Assess this cell for malaria.
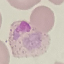

It is parasitized.

Acquired by smartphone through the microscope eyepiece. Giemsa-stained preparation. Cell patch, automatically extracted from a larger field of view and resized to 64 × 64 pixels. Thin blood smear.